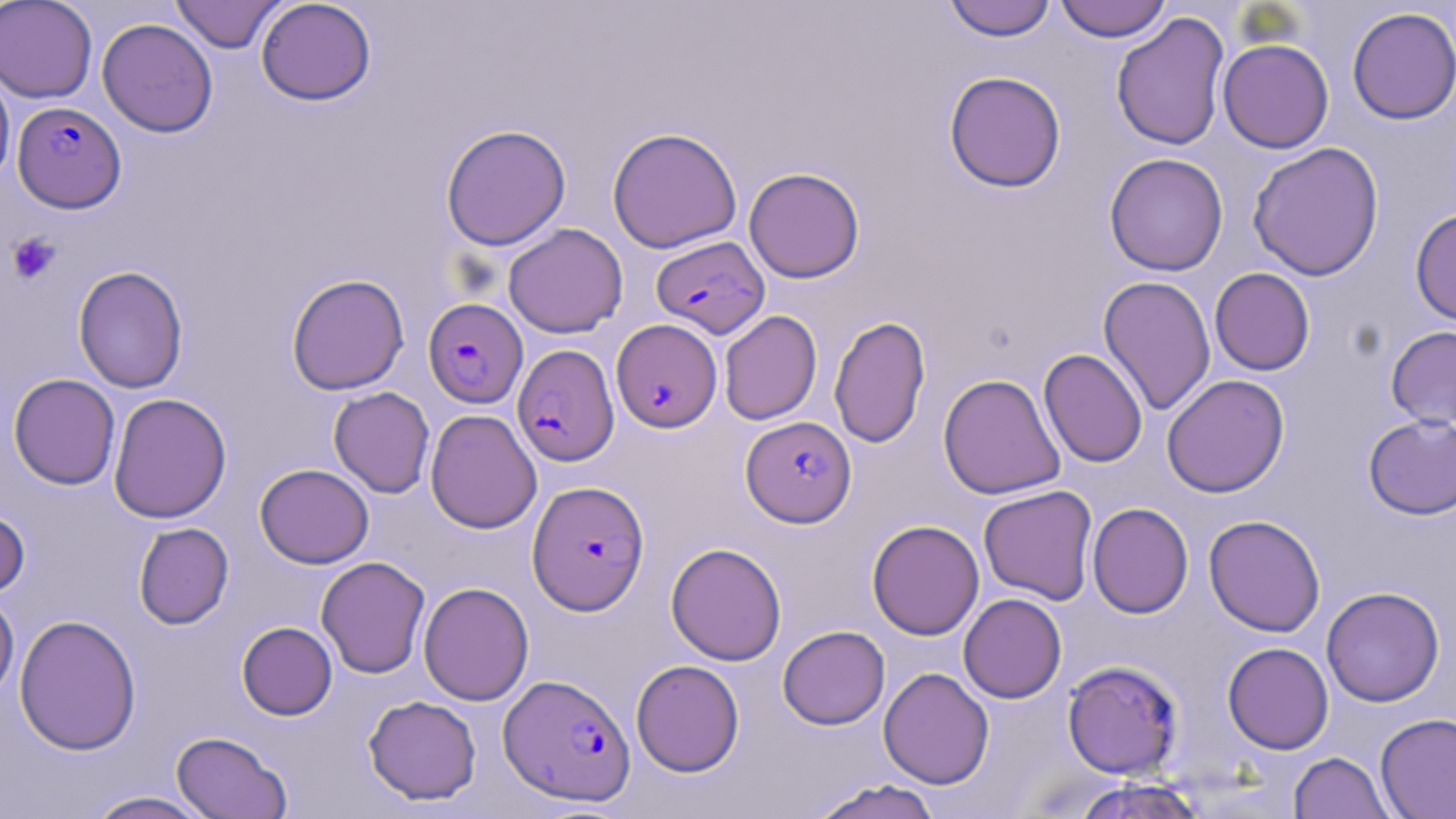

slide_level_diagnosis: Plasmodium falciparum
platelet_locations: 'approximate bounding boxes as (x1,y1)-(x2,y2) corner pairs in pixels: (6,232)-(62,285)'
image_size: 1456×819 pixels
modality: optical microscopy
preparation: thin blood smear
magnification: 1000x
uninfected_red_blood_cell_locations: 'approximate bounding boxes as (x1,y1)-(x2,y2) corner pairs in pixels: (0,0)-(97,103), (170,0)-(287,53), (256,0)-(377,106), (943,0)-(1056,41), (1054,0)-(1171,42), (1346,6)-(1456,124), (1111,12)-(1230,152), (97,18)-(218,137), (1217,38)-(1334,154), (0,65)-(15,190), (943,70)-(1067,193), (441,124)-(571,250), (607,126)-(743,253), (1247,141)-(1385,282), (1104,152)-(1228,276), (743,167)-(865,283), (1410,207)-(1456,327), (503,223)-(628,338), (73,265)-(188,393), (1210,267)-(1315,376), (286,273)-(410,395), (1098,275)-(1216,416), (719,310)-(822,425), (829,315)-(931,449), (1385,325)-(1456,430), (1038,348)-(1148,467), (9,373)-(121,490), (938,373)-(1066,500), (1161,374)-(1290,498), (329,387)-(435,498), (108,392)-(232,524), (425,409)-(542,533), (1363,413)-(1456,520), (255,463)-(374,568), (978,485)-(1098,605), (1087,502)-(1193,618), (0,503)-(31,600), (1203,514)-(1326,637), (867,520)-(984,640), (133,522)-(234,630), (666,542)-(786,666), (316,556)-(431,679), (418,581)-(534,706), (1321,586)-(1445,706), (0,590)-(19,705), (958,593)-(1067,703), (14,613)-(142,756), (237,621)-(337,720), (777,625)-(890,730), (1222,642)-(1334,754), (631,659)-(745,777), (1062,660)-(1185,780), (879,667)-(994,789), (364,695)-(482,805), (1375,712)-(1456,819), (171,731)-(292,818), (1289,752)-(1394,818), (1070,778)-(1211,819), (807,779)-(945,819), (83,791)-(217,818)'
plasmodium_falciparum_infected_red_blood_cell_locations: 'approximate bounding boxes as (x1,y1)-(x2,y2) corner pairs in pixels: (12,101)-(126,213), (651,235)-(769,338), (423,298)-(528,408), (611,319)-(722,433), (513,344)-(619,466), (741,416)-(856,527), (527,480)-(650,615), (499,673)-(636,806)'
field_of_view: single
stain: May-Grünwald-Giemsa